Assess this cell for malaria.
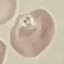

It is uninfected.

Summary:
  - Preparation: thin smear
  - Stain: Giemsa
  - Image type: cell patch, automatically extracted from a larger field of view and resized to 64 × 64 pixels
  - Capture: smartphone camera at the microscope eyepiece